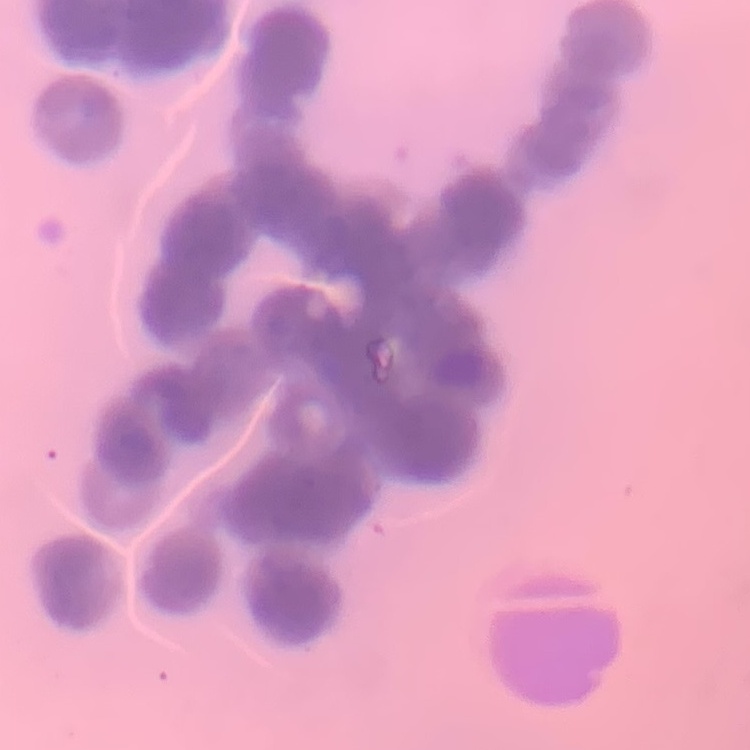 The red blood cells exhibit rouleaux formation. Thin peripheral smear. Square crop of a larger photomicrograph. Stained with either Field's or Giemsa.